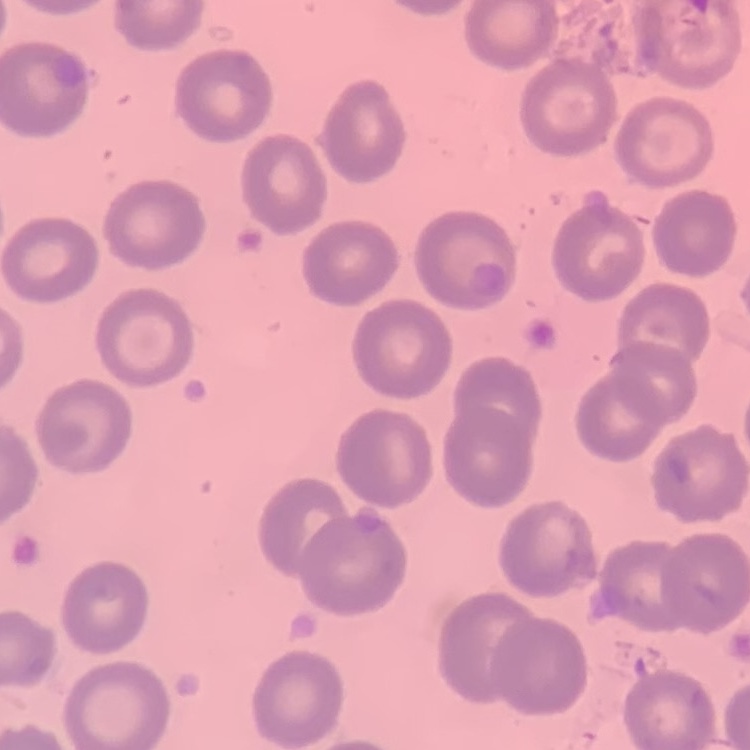
Summary:
  - Erythrocyte morphology: no rouleaux formation
  - Stain: Field's or Giemsa
  - Preparation: thin peripheral smear
  - Image type: square crop of a larger photomicrograph